Identify the blood parasite species.
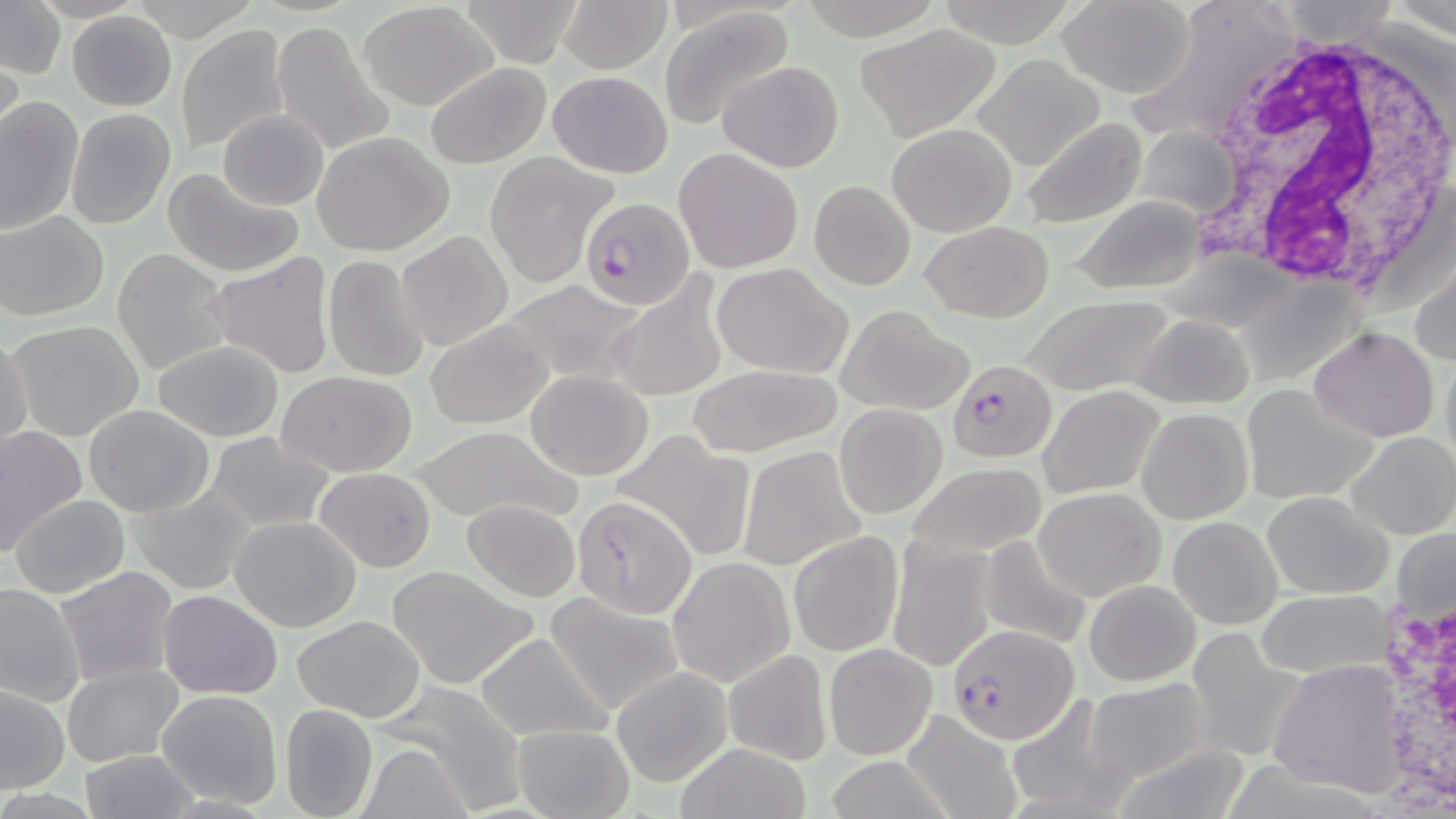

Plasmodium falciparum.

preparation = thin blood smear
field of view = one of a larger specimen
white blood cell locations = approximate bounding boxes as (x1, y1, x2, y2) in pixels: (1177, 27, 1456, 293), (1364, 570, 1456, 814)
uninfected red blood cell locations = approximate bounding boxes as (x1, y1, x2, y2) in pixels: (454, 0, 588, 67), (555, 0, 674, 73), (1056, 0, 1198, 99), (935, 1, 1074, 44), (1, 2, 64, 81), (357, 2, 501, 111), (1125, 3, 1296, 146), (658, 8, 796, 128), (68, 11, 177, 112), (268, 20, 396, 155), (173, 25, 291, 156), (854, 25, 1001, 141), (0, 54, 25, 157), (974, 54, 1105, 171), (716, 60, 844, 172), (424, 62, 552, 168), (546, 71, 673, 177), (0, 96, 85, 236), (65, 108, 175, 228), (216, 110, 329, 209), (1019, 117, 1147, 229), (886, 122, 1018, 236), (1136, 125, 1240, 223), (312, 131, 454, 256), (672, 147, 803, 275), (485, 153, 616, 286), (160, 165, 306, 278), (809, 181, 915, 290), (1068, 195, 1209, 294), (1, 210, 109, 320), (921, 220, 1055, 323), (397, 230, 513, 352), (113, 249, 232, 376), (201, 250, 336, 381), (1410, 253, 1456, 370), (322, 255, 429, 384), (713, 263, 853, 380), (601, 274, 729, 404), (498, 278, 650, 386), (1017, 295, 1178, 399), (836, 307, 970, 416), (1133, 314, 1254, 410), (6, 318, 145, 442), (425, 318, 555, 429), (1307, 327, 1439, 443), (0, 331, 33, 454), (154, 341, 284, 442), (1440, 346, 1456, 477), (691, 366, 838, 458), (523, 369, 655, 480), (278, 370, 417, 476), (1240, 382, 1375, 504), (1038, 385, 1165, 499), (834, 403, 948, 519), (83, 405, 216, 517), (1137, 408, 1253, 525), (409, 426, 581, 526), (0, 427, 84, 553), (202, 431, 337, 532), (611, 431, 756, 561), (1348, 431, 1456, 540), (738, 445, 867, 571), (902, 463, 1047, 559), (314, 467, 436, 573), (127, 484, 256, 597), (1033, 486, 1165, 600), (1263, 491, 1393, 598), (10, 493, 129, 599), (462, 499, 581, 601), (578, 499, 694, 618), (231, 516, 362, 632), (1168, 516, 1281, 629), (1392, 528, 1455, 625), (788, 531, 904, 657), (978, 535, 1094, 650), (885, 536, 997, 672), (668, 555, 796, 688), (385, 564, 541, 691), (54, 565, 183, 686), (1084, 580, 1200, 686), (1, 582, 86, 707), (156, 589, 283, 700), (1256, 589, 1393, 679), (543, 592, 689, 716), (291, 614, 427, 721), (1186, 627, 1304, 761), (473, 631, 613, 742), (824, 643, 937, 758), (722, 648, 835, 765), (1267, 659, 1412, 795), (62, 665, 184, 767), (610, 667, 733, 787), (1084, 678, 1207, 782), (376, 683, 526, 811), (0, 686, 69, 794), (156, 689, 283, 809), (1006, 692, 1140, 816), (280, 703, 378, 819), (901, 708, 1022, 819), (510, 725, 636, 818), (1114, 739, 1253, 818), (355, 742, 473, 819), (675, 743, 814, 819), (78, 749, 199, 818), (819, 757, 958, 818)
modality = optical microscopy
image size = 1456×819 pixels
stain = May-Grünwald-Giemsa
magnification = 1000x
Plasmodium falciparum-infected red blood cell locations = approximate bounding boxes as (x1, y1, x2, y2) in pixels: (579, 197, 696, 310), (948, 359, 1054, 463), (944, 623, 1077, 743)